Name the parasite shown.
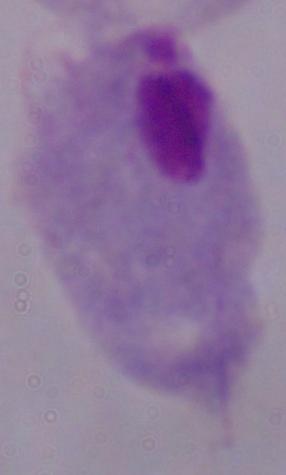

This is a trichomonad.

Summary:
  - Modality: photomicrograph
  - Magnification: 1000x